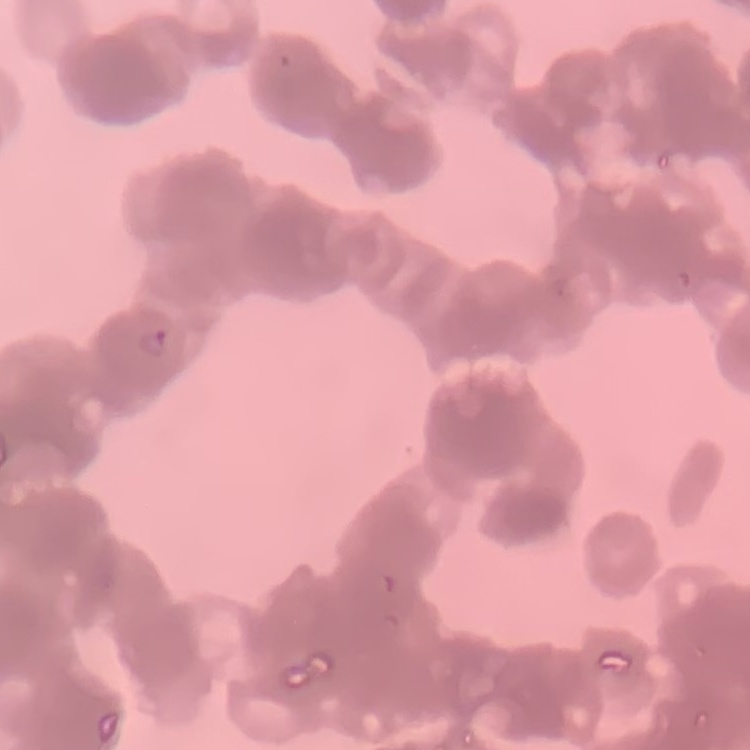
Summary:
  - Red blood cell morphology: rouleaux formation
  - Stain: Field's or Giemsa
  - Preparation: thin blood smear
  - Image type: square crop of a larger photomicrograph